Name the parasite shown.
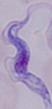
This is a trypanosome.

magnification = 1000x
modality = micrograph